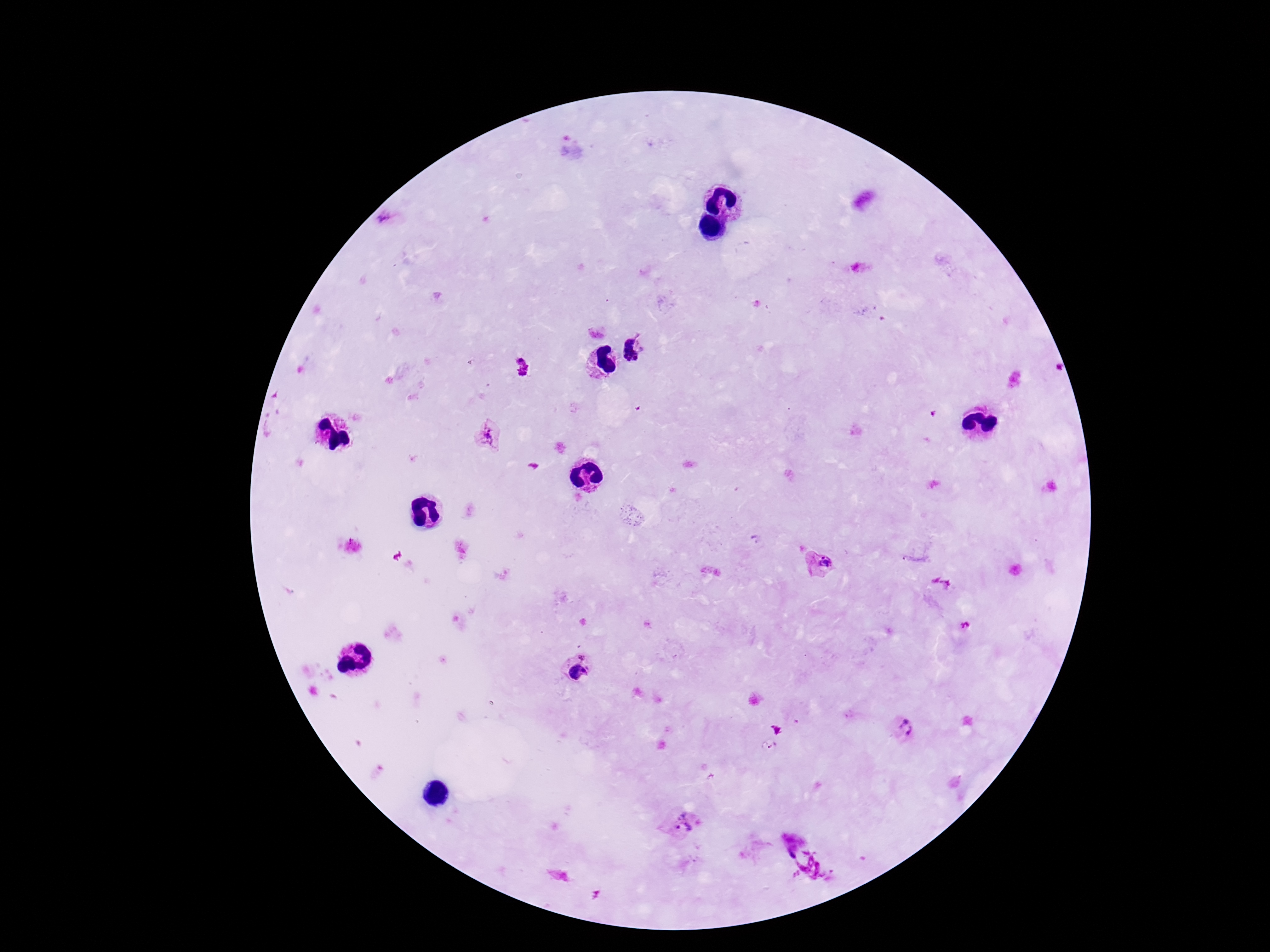
magnification = 100x
capture = smartphone camera through the microscope eyepiece
stain = Giemsa
image size = 1270×952 pixels
preparation = thick blood film
patient malaria status = positive
Plasmodium parasite locations = approximate centers as (x, y) in pixels: (639, 347), (522, 367), (489, 436), (820, 565), (583, 656), (578, 672), (904, 727), (683, 823), (793, 847)
field of view = one from this slide